Assess this cell for malaria.
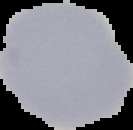
Uninfected.

Cell region segmented out of the field of view; the surrounding area is masked to black. Image is 133×130 pixels. From a thin blood film.